Assess this cell for malaria.
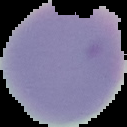
It is uninfected.

Summary:
  - Image type: segmented cell region with the area outside set to black
  - Image size: 127×127 pixels
  - Preparation: thin blood smear